Draw a bounding box around every malaria parasite.
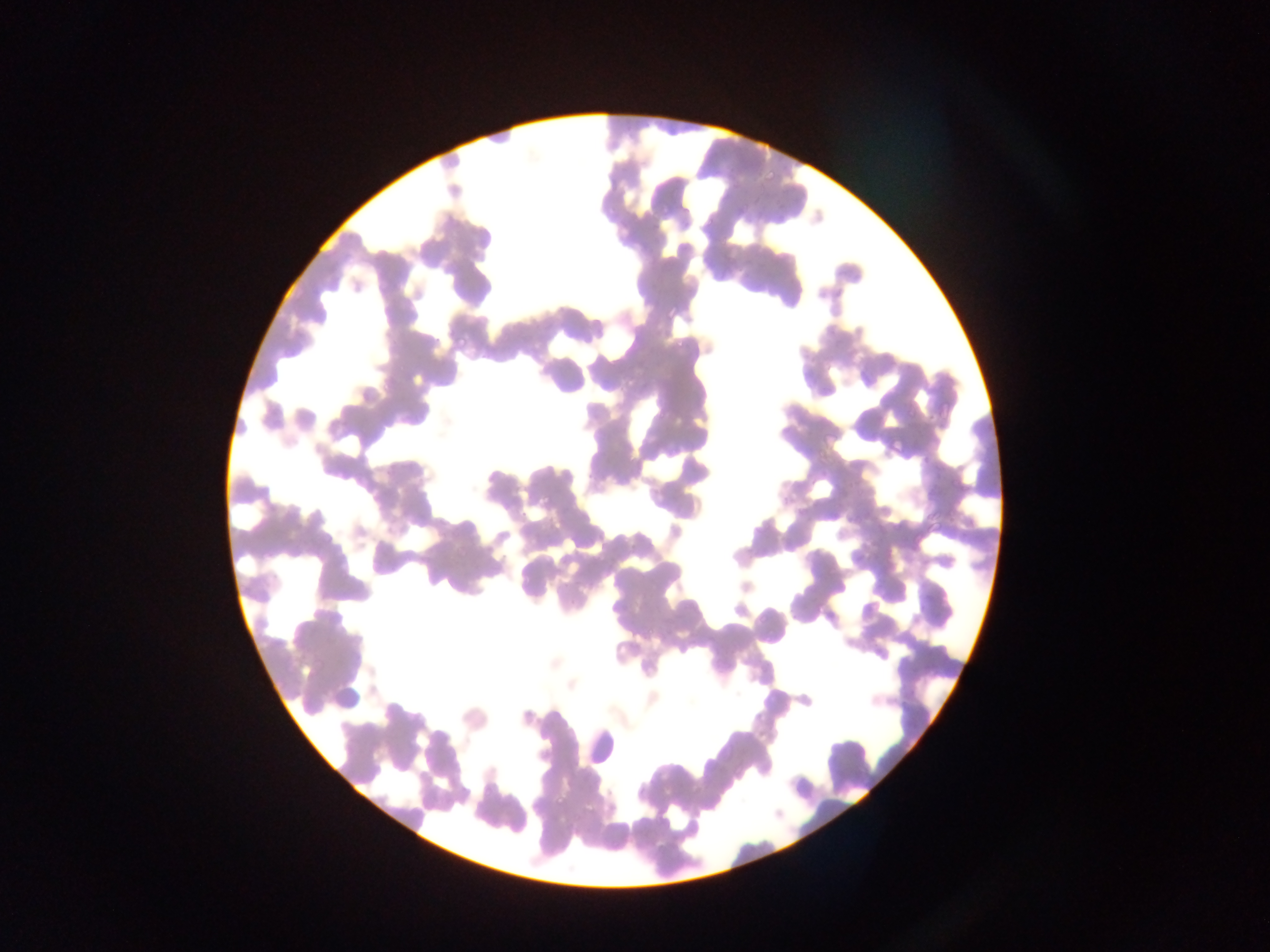

Approximate bounding boxes as {left, top, right, bottom} in pixels.
Malaria parasites: {763, 171, 776, 184}, {733, 202, 747, 216}, {657, 204, 671, 219}, {602, 206, 612, 215}, {676, 206, 692, 225}, {774, 207, 789, 222}, {774, 214, 786, 226}, {703, 216, 715, 230}, {664, 305, 678, 319}, {455, 334, 469, 349}, {671, 335, 688, 351}, {886, 437, 902, 454}, {450, 546, 462, 559}, {555, 795, 568, 809}, {548, 796, 565, 811}.

Image is 1270×952 pixels. Thin blood film. Sample from Ghana. Single field of view. Photographed through a microscope with a mobile-phone camera.